Report the malaria status of this cell.
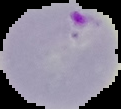
Parasitized.

preparation = thin blood film
image size = 121×109 pixels
image type = segmented cell region on a black background